Give the extent of all uninfected red blood cells.
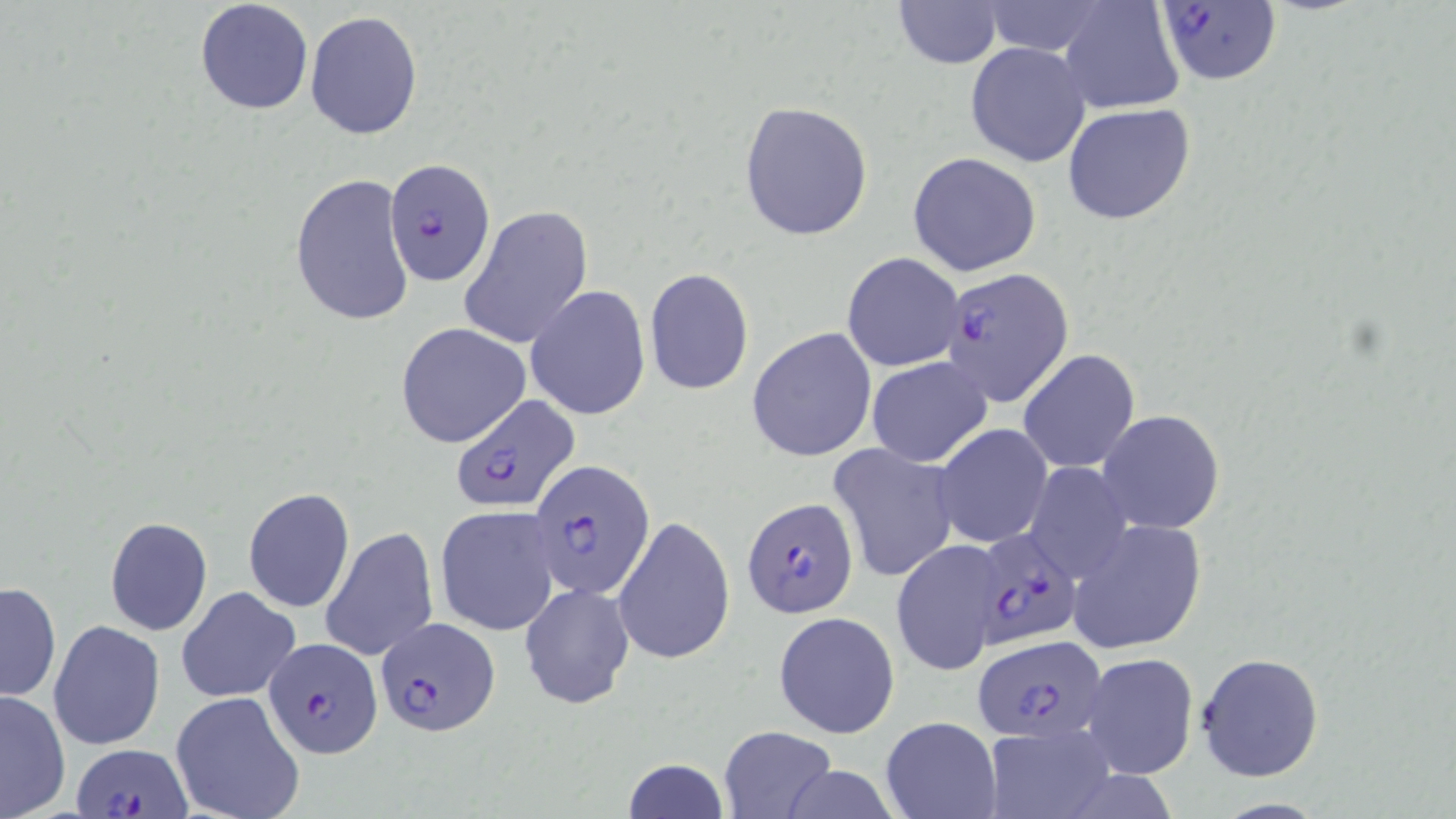

Approximate bounding boxes as [x1, y1, x2, y2] in pixels.
Uninfected red blood cells: [193, 1, 314, 116], [890, 1, 1004, 68], [1058, 1, 1184, 115], [304, 10, 423, 142], [965, 42, 1091, 167], [738, 100, 875, 241], [1063, 103, 1197, 226], [908, 152, 1041, 276], [290, 173, 417, 329], [460, 206, 593, 349], [841, 252, 963, 372], [644, 267, 754, 396], [525, 285, 651, 421], [395, 323, 530, 448], [747, 328, 876, 463], [1019, 349, 1140, 473], [866, 356, 992, 467], [1097, 409, 1225, 534], [934, 423, 1051, 547], [829, 443, 960, 584], [1023, 462, 1133, 584], [243, 487, 354, 613], [435, 506, 561, 636], [613, 515, 735, 667], [103, 516, 213, 635], [1067, 519, 1207, 655], [321, 526, 439, 661], [891, 538, 1005, 677], [1, 580, 61, 704], [519, 583, 633, 709], [177, 586, 301, 704], [774, 611, 900, 740], [49, 619, 166, 749], [1195, 651, 1324, 781], [1080, 652, 1199, 780], [0, 689, 71, 819], [171, 692, 307, 819], [880, 716, 1001, 819], [980, 723, 1117, 819], [718, 726, 837, 817], [621, 757, 730, 819].

Summary:
  - Plasmodium falciparum-infected red blood cell locations: [1168, 2, 1287, 88], [383, 157, 496, 288], [939, 266, 1076, 409], [448, 393, 578, 513], [530, 459, 653, 599], [742, 498, 859, 620], [979, 529, 1091, 645], [375, 615, 499, 734], [974, 636, 1109, 741], [263, 638, 381, 758], [73, 742, 189, 816]
  - Slide-level diagnosis: Plasmodium falciparum
  - Modality: optical microscopy
  - Field of view: one of a larger specimen
  - Stain: May-Grünwald-Giemsa
  - Magnification: 1000x
  - Preparation: thin blood smear
  - Image size: 1456×819 pixels